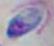

Micrograph. Toxoplasma gondii is shown. Captured at 1000x magnification.